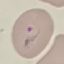

Result: malaria parasites identified. Giemsa stain. Automatically extracted cell patch, resized to 64 × 64 pixels. Thin blood smear. Acquired by smartphone through the microscope eyepiece.